Classify this cell by malaria status.
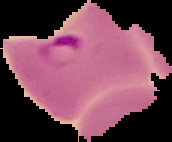

Parasitized.

image_type: cell region segmented out of the field of view; surrounding area masked to black
image_size: 172×142 pixels
preparation: thin blood smear